State which parasite is depicted.
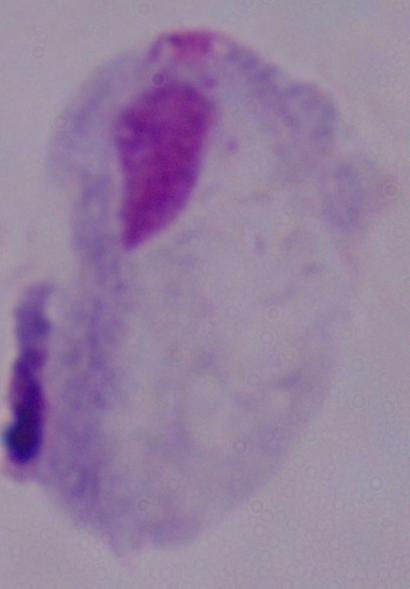

A trichomonad.

Captured at 1000x magnification. Photomicrograph.